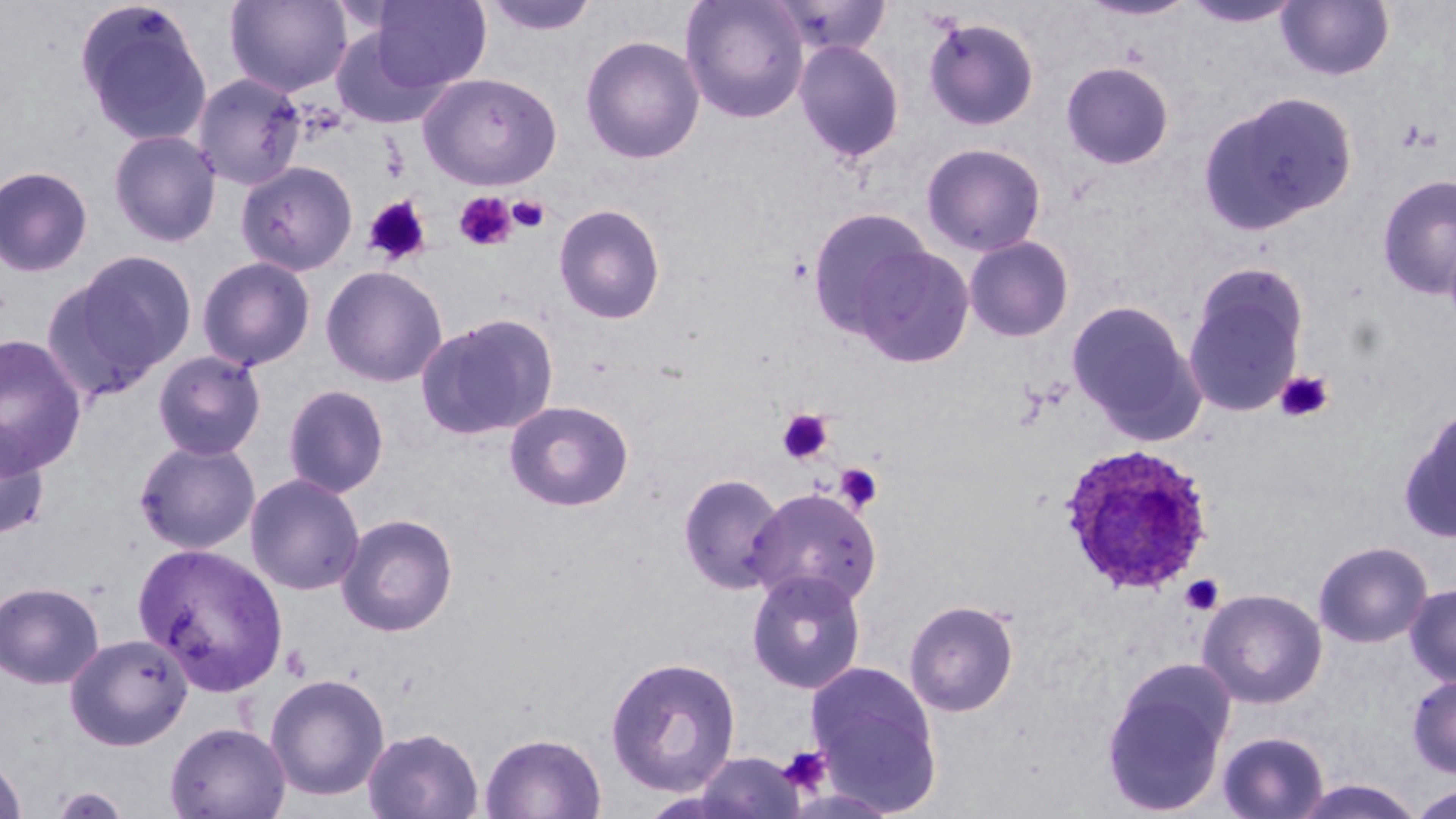

Summary:
  - Coordinate format: approximate bounding boxes as [x1, y1, x2, y2] in pixels
  - Platelet locations: [453, 191, 518, 251], [508, 195, 550, 233], [363, 196, 432, 266], [1275, 370, 1334, 422], [778, 409, 835, 465], [834, 463, 883, 513], [1181, 574, 1224, 615], [777, 745, 833, 795]
  - Uninfected red blood cell locations: [73, 0, 214, 148], [363, 0, 492, 94], [481, 0, 601, 37], [680, 0, 810, 124], [769, 0, 892, 59], [1180, 0, 1305, 29], [225, 1, 352, 97], [1078, 1, 1196, 23], [1277, 1, 1394, 81], [922, 16, 1041, 131], [328, 21, 456, 128], [580, 34, 705, 164], [793, 39, 905, 164], [1061, 60, 1175, 170], [418, 71, 562, 190], [192, 72, 307, 190], [1200, 91, 1357, 235], [108, 129, 222, 247], [921, 142, 1047, 256], [236, 161, 358, 275], [0, 165, 94, 277], [1377, 174, 1456, 300], [553, 203, 666, 325], [807, 207, 935, 340], [963, 235, 1075, 342], [850, 243, 975, 368], [55, 250, 198, 388], [196, 256, 316, 371], [320, 265, 448, 387], [1183, 266, 1309, 418], [1066, 300, 1205, 443], [415, 313, 558, 441], [0, 334, 89, 476], [152, 350, 267, 460], [283, 385, 389, 498], [504, 400, 634, 512], [1399, 404, 1456, 542], [0, 418, 50, 542], [134, 437, 261, 554], [677, 472, 785, 594], [245, 474, 366, 596], [747, 487, 881, 611], [336, 513, 459, 637], [1314, 540, 1432, 648], [133, 541, 289, 695], [746, 569, 867, 694], [0, 581, 105, 689], [1404, 583, 1456, 688], [1198, 588, 1327, 708], [904, 599, 1019, 716], [64, 632, 193, 751], [604, 655, 741, 797], [1102, 659, 1235, 816], [805, 660, 943, 813], [264, 672, 390, 803], [1408, 674, 1456, 778], [165, 721, 291, 819], [362, 727, 484, 819], [1216, 731, 1330, 819], [479, 732, 607, 819], [689, 751, 806, 818], [0, 752, 28, 819], [1290, 779, 1426, 819], [1407, 782, 1456, 818], [51, 786, 130, 818]
  - Plasmodium ovale-infected red blood cell locations: [1058, 442, 1215, 595]
  - Slide-level diagnosis: Plasmodium ovale
  - Image size: 1456×819 pixels
  - Magnification: 1000x
  - Modality: light microscopy
  - Field of view: single
  - Stain: May-Grünwald-Giemsa
  - Preparation: thin blood film